Identify the parasite.
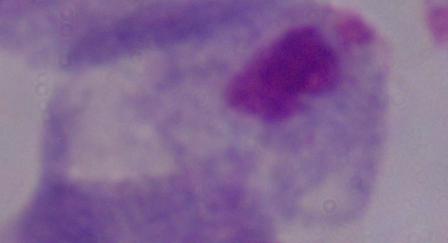
This is a trichomonad.

{
  "magnification": "1000x",
  "modality": "micrograph"
}